Report the malaria status of this cell.
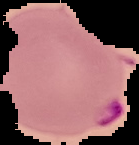

Parasitized.

From a thin blood film. The area outside the segmented cell region is set to black. Image is 139×145 pixels.